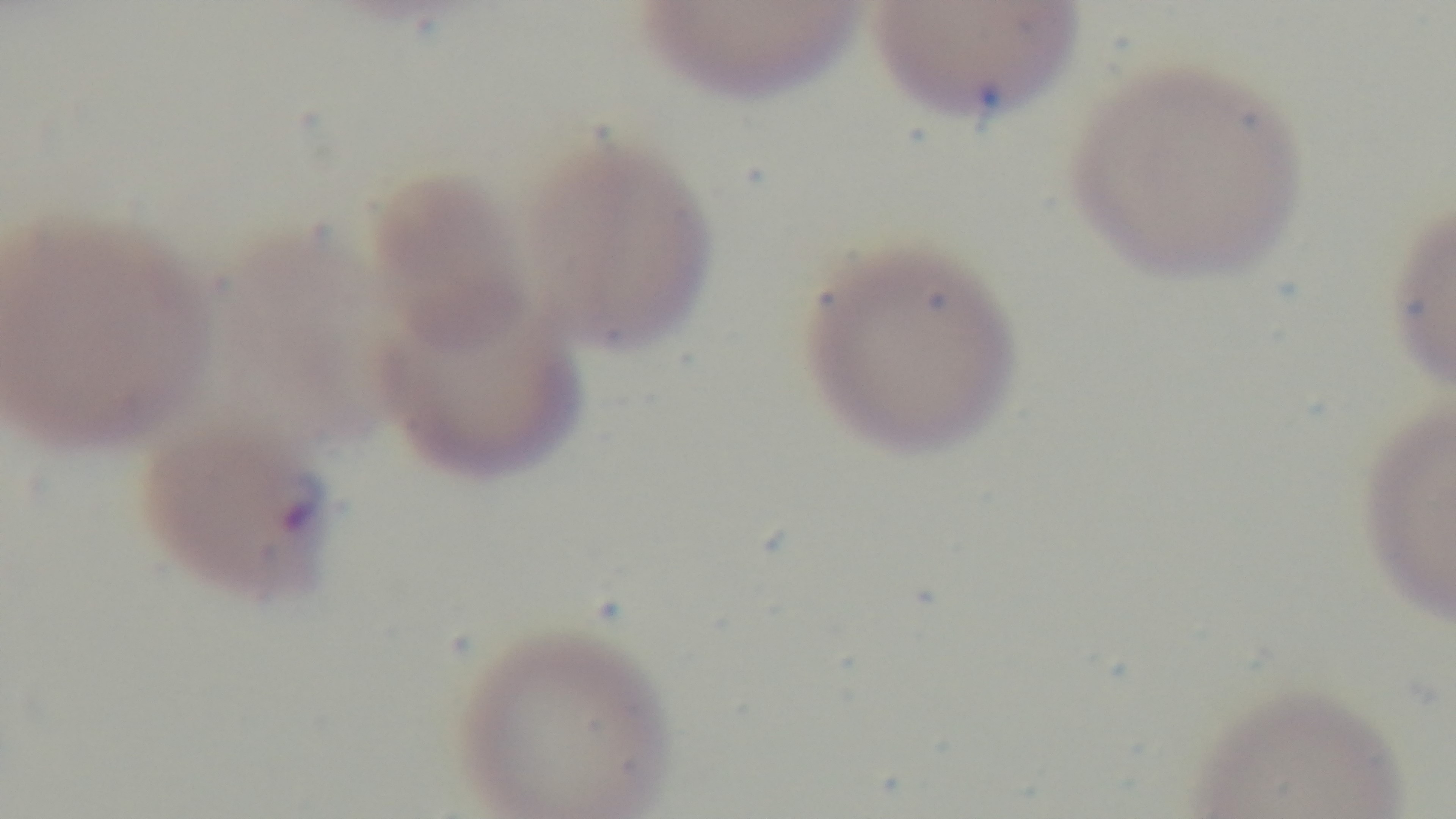

malaria status = infected
modality = light microscopy
field of view = single
capture = mounted 4K digital camera
preparation = thin blood film
objective = 100x oil immersion
stain = Giemsa